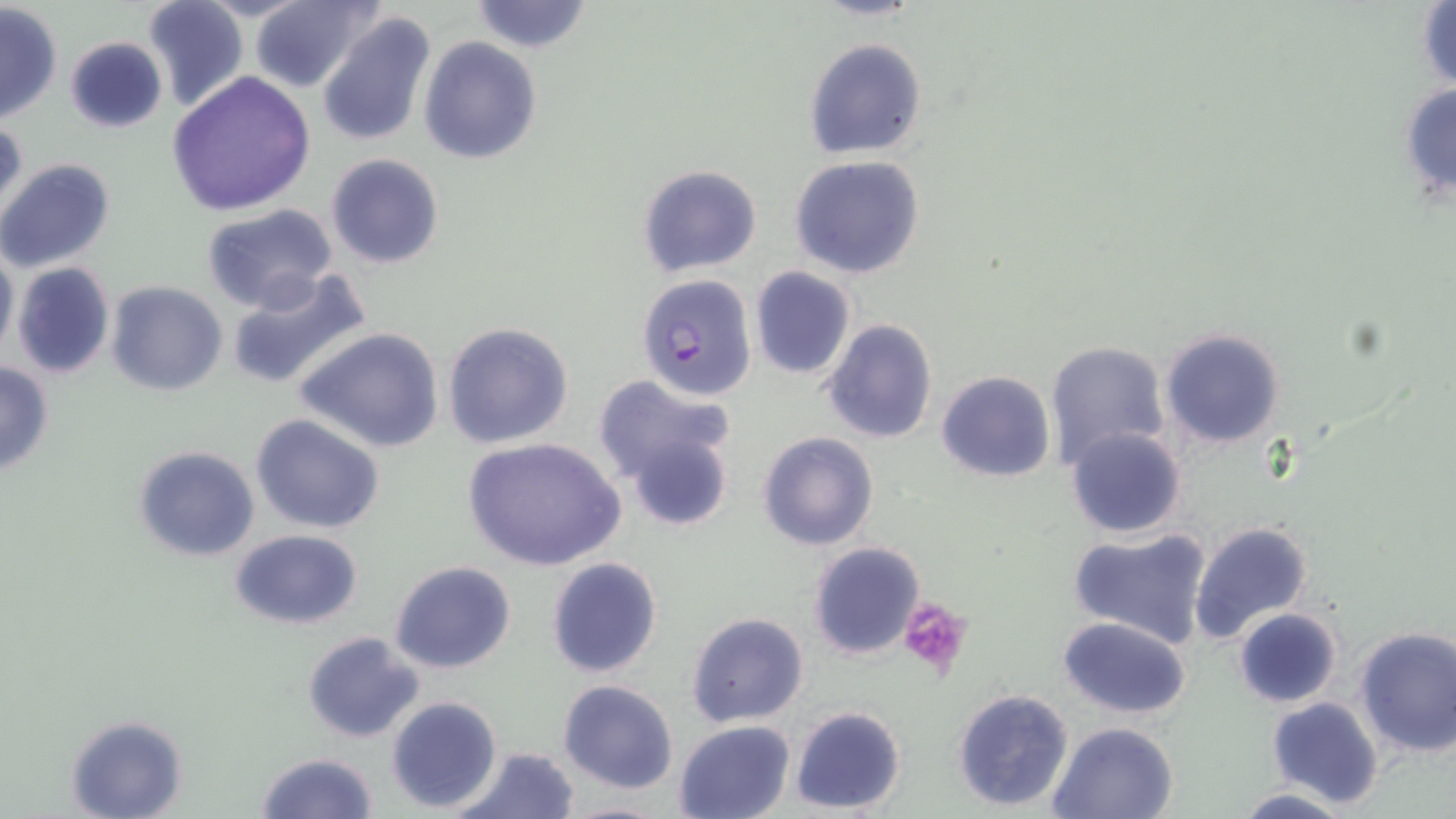
Summary:
  - Coordinate format: approximate bounding boxes as (x1,y1)-(x2,y2) corner pairs in pixels
  - Uninfected red blood cell locations: (250,0)-(381,92), (467,0)-(595,53), (809,0)-(927,21), (141,1)-(248,113), (1,3)-(62,123), (1415,3)-(1455,93), (317,10)-(435,148), (64,36)-(169,134), (420,37)-(542,165), (804,38)-(927,158), (167,71)-(315,215), (1397,80)-(1456,204), (1,117)-(28,228), (325,153)-(444,270), (790,155)-(927,280), (0,159)-(117,273), (638,164)-(762,277), (202,204)-(337,313), (0,242)-(18,361), (11,261)-(114,380), (750,266)-(856,380), (225,268)-(371,395), (105,280)-(228,397), (821,318)-(937,444), (441,321)-(574,449), (296,325)-(446,452), (1159,327)-(1286,450), (1043,341)-(1170,470), (0,361)-(54,479), (935,371)-(1055,481), (591,374)-(737,489), (250,414)-(385,534), (1065,427)-(1187,538), (757,431)-(879,551), (625,433)-(734,531), (462,436)-(625,575), (133,446)-(259,562), (1187,521)-(1313,646), (1065,526)-(1214,650), (229,528)-(364,629), (808,542)-(926,661), (545,556)-(664,679), (390,561)-(516,674), (1232,607)-(1343,709), (687,611)-(810,728), (1058,616)-(1192,718), (1352,627)-(1456,759), (302,631)-(425,743), (557,680)-(681,795), (951,688)-(1074,811), (386,695)-(503,811), (1265,696)-(1383,809), (790,705)-(907,815), (66,715)-(186,819), (674,720)-(797,818), (1049,721)-(1179,819), (454,746)-(581,819), (255,751)-(380,819), (1231,787)-(1357,818), (552,800)-(674,819)
  - Plasmodium falciparum-infected red blood cell locations: (636,273)-(758,401)
  - Platelet locations: (898,599)-(973,676)
  - Slide-level diagnosis: Plasmodium falciparum
  - Modality: light microscopy
  - Field of view: single
  - Magnification: 1000x
  - Image size: 1456×819 pixels
  - Stain: May-Grünwald-Giemsa
  - Preparation: thin blood smear